Identify the parasite.
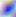

This is Toxoplasma gondii.

400x magnification. Micrograph.